Comment on the morphology of the erythrocytes.
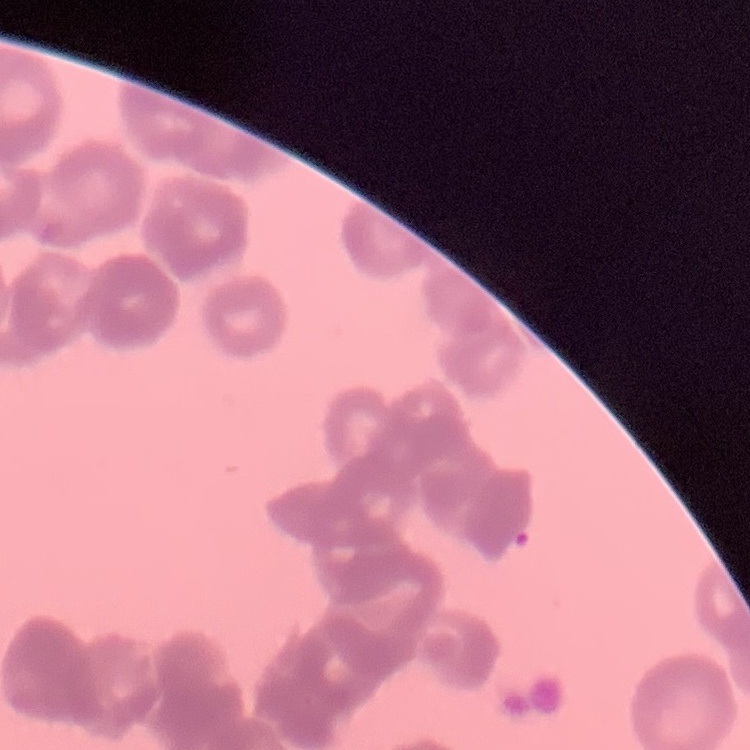
They show rouleaux formation.

Field's or Giemsa stain. Square crop of a larger photomicrograph. Thin peripheral smear.